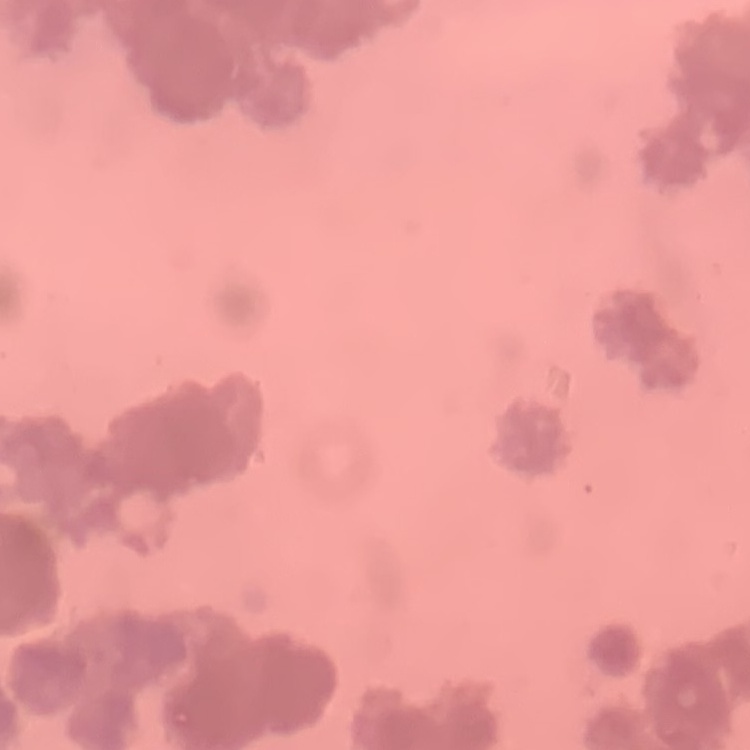

Summary:
  - Erythrocyte morphology: rouleaux formation
  - Preparation: thin blood smear
  - Image type: one tile cut from a larger photomicrograph
  - Stain: Field's or Giemsa